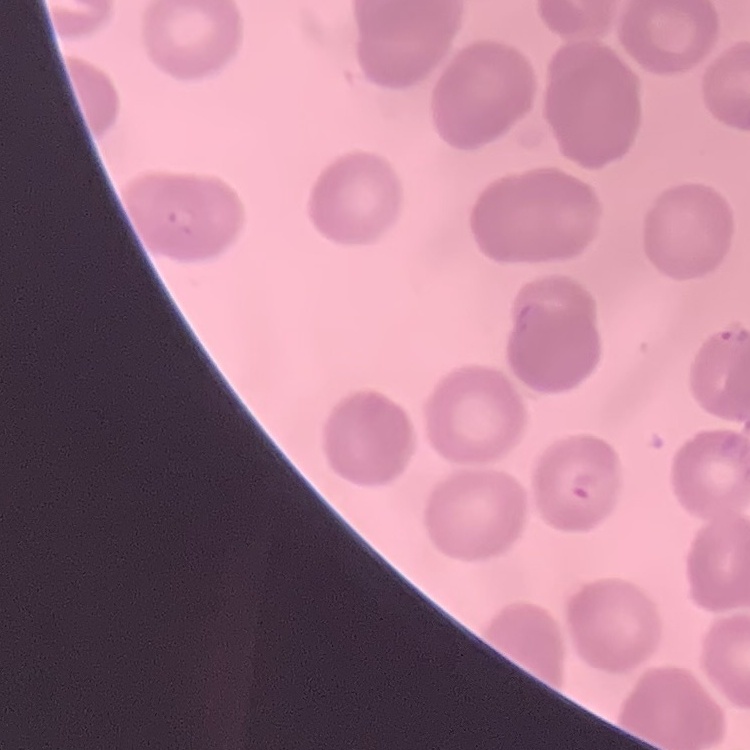

red blood cell morphology = no rouleaux formation
image type = square crop of a larger photomicrograph
stain = Field's or Giemsa
preparation = thin peripheral smear